Report the malaria status of this cell.
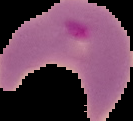
It is parasitized.

From a thin blood film. Image is 133×121 pixels. The area outside the segmented cell region is set to black.